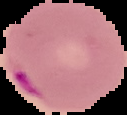
From a thin blood film. Image is 127×115 pixels. Malaria status: parasitized. Segmented cell region on a black background.